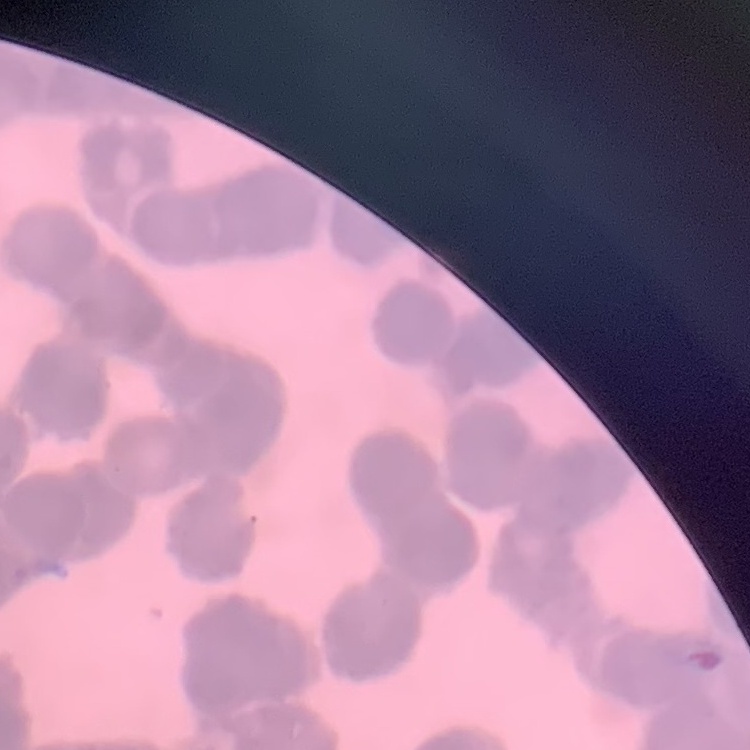 The red blood cells exhibit rouleaux formation. One tile cut from a larger photomicrograph. Thin blood film. Stained with either Field's or Giemsa.